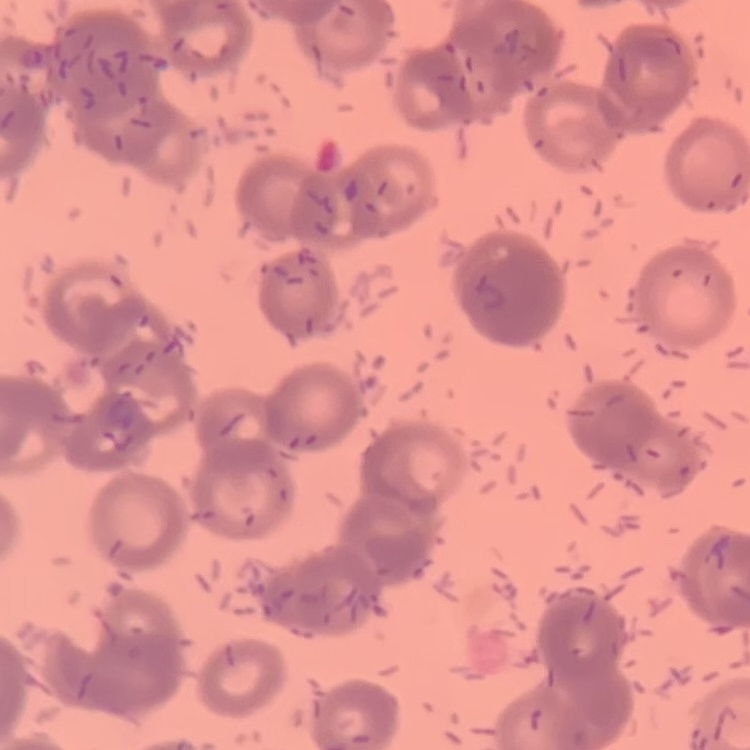

The red blood cells exhibit rouleaux formation. Square crop of a larger photomicrograph. Thin peripheral smear. Stained with either Field's or Giemsa.